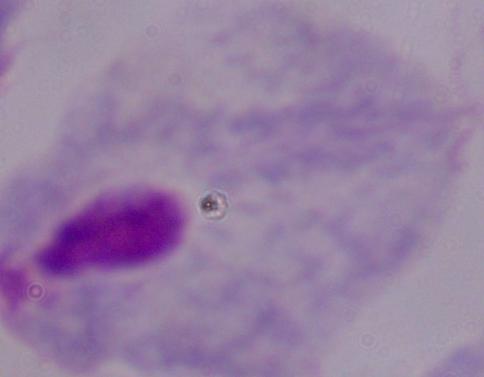
A trichomonad is shown. Captured at 1000x magnification. Photomicrograph.